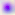

Summary:
  - Modality: micrograph
  - Identification: Toxoplasma gondii
  - Magnification: 400x